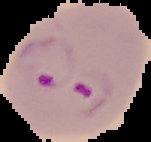 Image is 151×142 pixels. Result: Plasmodium parasites detected. The area outside the segmented cell region is set to black. From a thin blood smear.